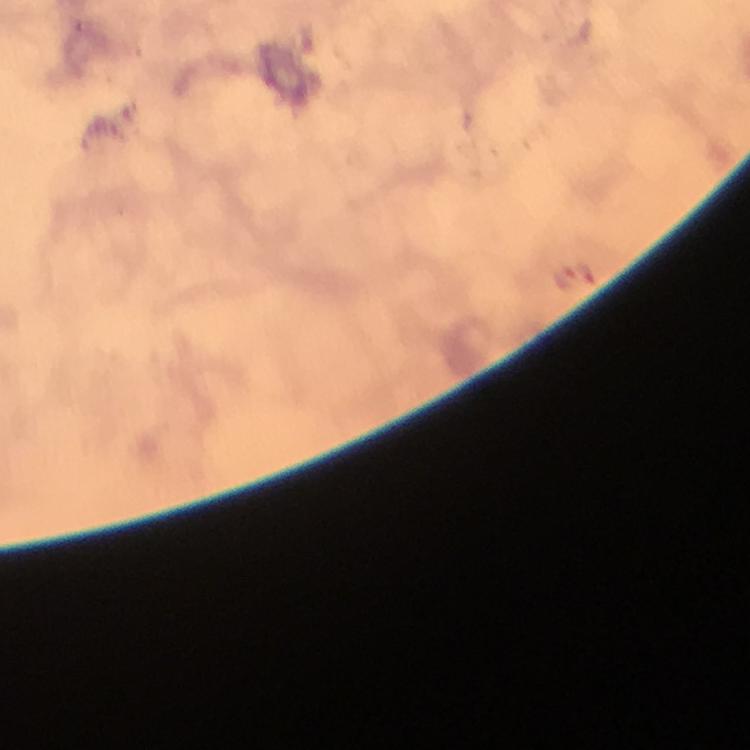

Approximate centers as {x, y} in pixels. Plasmodium parasite locations: {586, 271}, {561, 277}. Giemsa stain. At 100x magnification. Immersion oil was used. Image is 750×750 pixels. From a malaria diagnostic workup. Thick smear. A crop from one field of view. Smartphone photograph taken through a microscope.